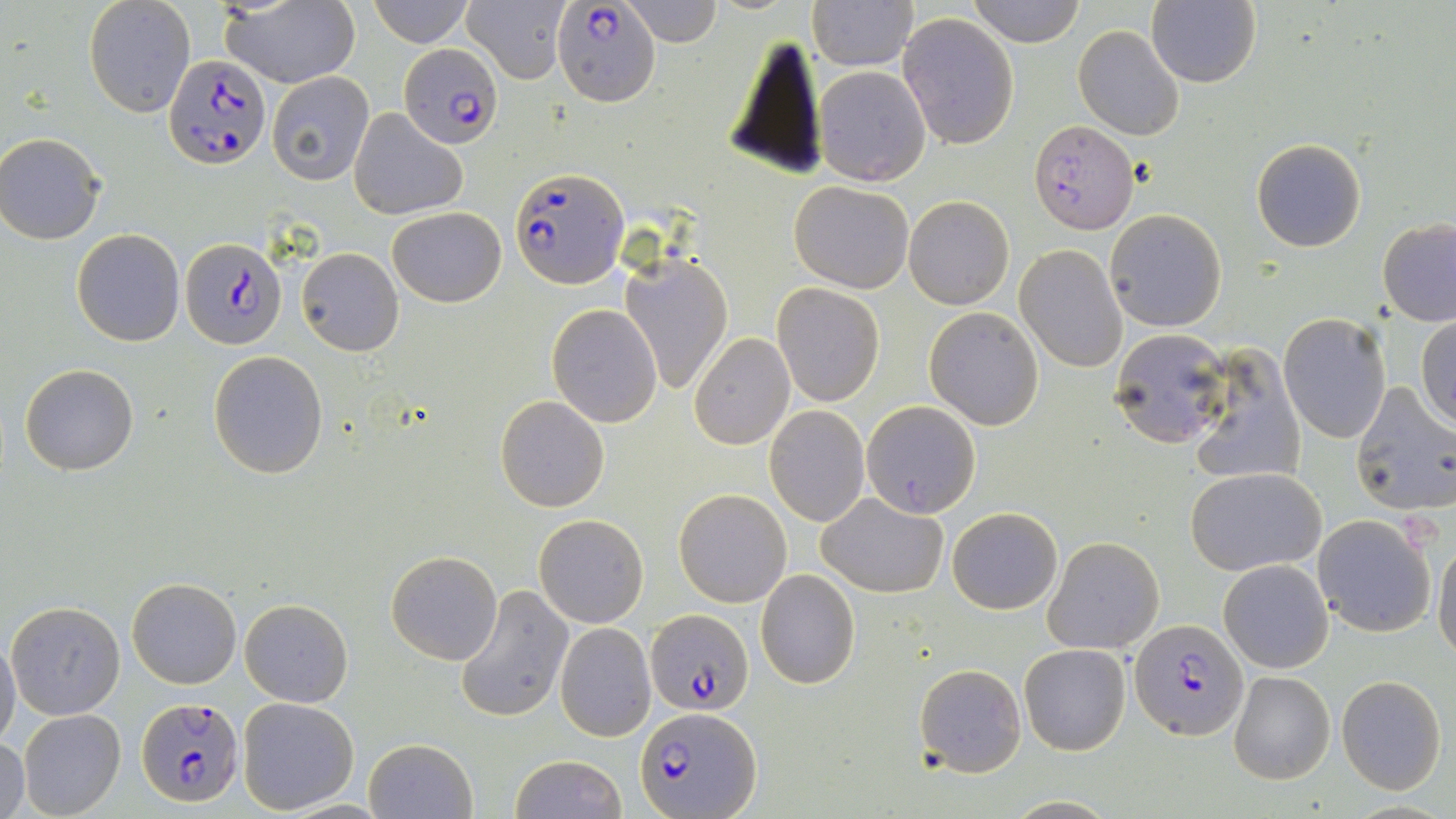
slide-level diagnosis = Plasmodium falciparum
image size = 1456×819 pixels
field of view = one of a larger specimen
magnification = 1000x
stain = May-Grünwald-Giemsa
Plasmodium falciparum-infected red blood cell locations = approximate bounding boxes as (x1, y1, x2, y2) in pixels: (553, 2, 661, 105), (399, 41, 502, 149), (165, 54, 270, 170), (1030, 120, 1138, 233), (511, 165, 628, 290), (180, 238, 284, 349), (644, 609, 754, 716), (1131, 619, 1246, 740), (137, 696, 244, 810), (636, 703, 762, 818)
platelet locations = approximate bounding boxes as (x1, y1, x2, y2) in pixels: (1406, 515, 1438, 553)
preparation = thin blood smear
modality = optical microscopy
uninfected red blood cell locations = approximate bounding boxes as (x1, y1, x2, y2) in pixels: (83, 0, 195, 117), (215, 0, 360, 88), (368, 0, 472, 47), (619, 0, 723, 47), (968, 0, 1085, 47), (1148, 0, 1263, 88), (463, 1, 570, 85), (808, 1, 918, 71), (896, 12, 1019, 151), (1073, 24, 1184, 141), (722, 30, 827, 179), (813, 65, 931, 187), (267, 72, 374, 184), (347, 108, 468, 221), (0, 135, 105, 244), (1251, 137, 1367, 253), (789, 180, 913, 293), (904, 195, 1013, 309), (388, 206, 506, 307), (1105, 209, 1226, 331), (1376, 217, 1456, 327), (72, 229, 187, 347), (1018, 229, 1223, 355), (1014, 244, 1127, 373), (296, 248, 404, 355), (620, 252, 733, 395), (772, 283, 884, 405), (547, 304, 663, 428), (923, 307, 1044, 430), (1279, 313, 1391, 443), (1417, 314, 1456, 429), (1108, 327, 1232, 451), (689, 332, 795, 449), (1188, 345, 1305, 487), (208, 349, 328, 478), (19, 363, 139, 476), (1348, 383, 1456, 517), (495, 395, 610, 513), (862, 401, 980, 518), (765, 405, 870, 526), (1185, 467, 1325, 575), (674, 489, 791, 608), (817, 494, 948, 597), (947, 507, 1062, 614), (1311, 513, 1436, 639), (534, 514, 648, 627), (1043, 536, 1164, 654), (1432, 537, 1456, 662), (386, 550, 503, 664), (1219, 559, 1334, 674), (755, 569, 861, 690), (128, 577, 241, 688), (455, 584, 575, 723), (240, 599, 353, 707), (6, 600, 126, 720), (555, 622, 656, 742), (0, 636, 21, 751), (1018, 643, 1131, 755), (914, 663, 1025, 776), (1227, 671, 1335, 785), (1336, 675, 1447, 793), (237, 696, 361, 812), (18, 709, 126, 819), (1, 734, 29, 819), (364, 738, 477, 819), (510, 754, 627, 819)